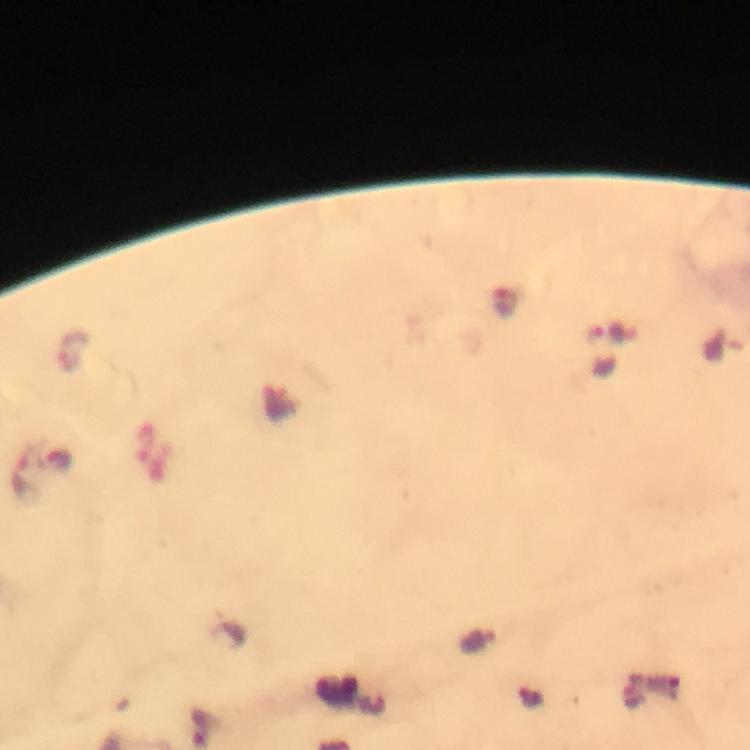
{
  "context": "from a malaria diagnostic workup",
  "malaria_parasite_locations": "approximate centers as {x, y} in pixels: {73, 352}",
  "capture": "smartphone camera through the microscope",
  "immersion_oil": "used",
  "image_size": "750×750 pixels",
  "stain": "Giemsa",
  "preparation": "thick blood film",
  "cropped_from": "a single field of view",
  "magnification": "100x"
}